Classify this cell by malaria status.
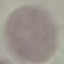

Uninfected.

Summary:
  - Stain: Giemsa
  - Image type: cell patch, automatically extracted from a larger field of view and resized to 64 × 64 pixels
  - Capture: smartphone camera at the microscope eyepiece
  - Preparation: thin smear